Assess this cell for malaria.
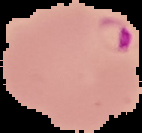
It is parasitized.

From a thin blood film. Image is 142×133 pixels. The area outside the segmented cell region is set to black.